Report the malaria status of this cell.
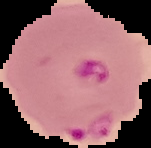

Parasitized.

Summary:
  - Image size: 151×148 pixels
  - Preparation: thin blood film
  - Image type: segmented cell region with the area outside set to black